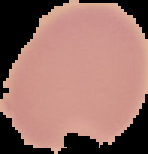
preparation = thin blood film
image type = segmented cell region on a black background
result = negative for Plasmodium parasites
image size = 148×154 pixels